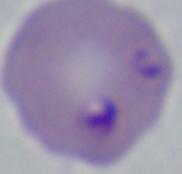

identification = Babesia
modality = photomicrograph
magnification = 1000x